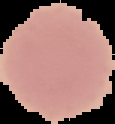

The area outside the segmented cell region is set to black. Malaria status: uninfected. From a thin blood film. Image is 115×124 pixels.